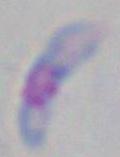 Micrograph. 1000x magnification. Toxoplasma gondii is seen.